Evaluate for Plasmodium parasites.
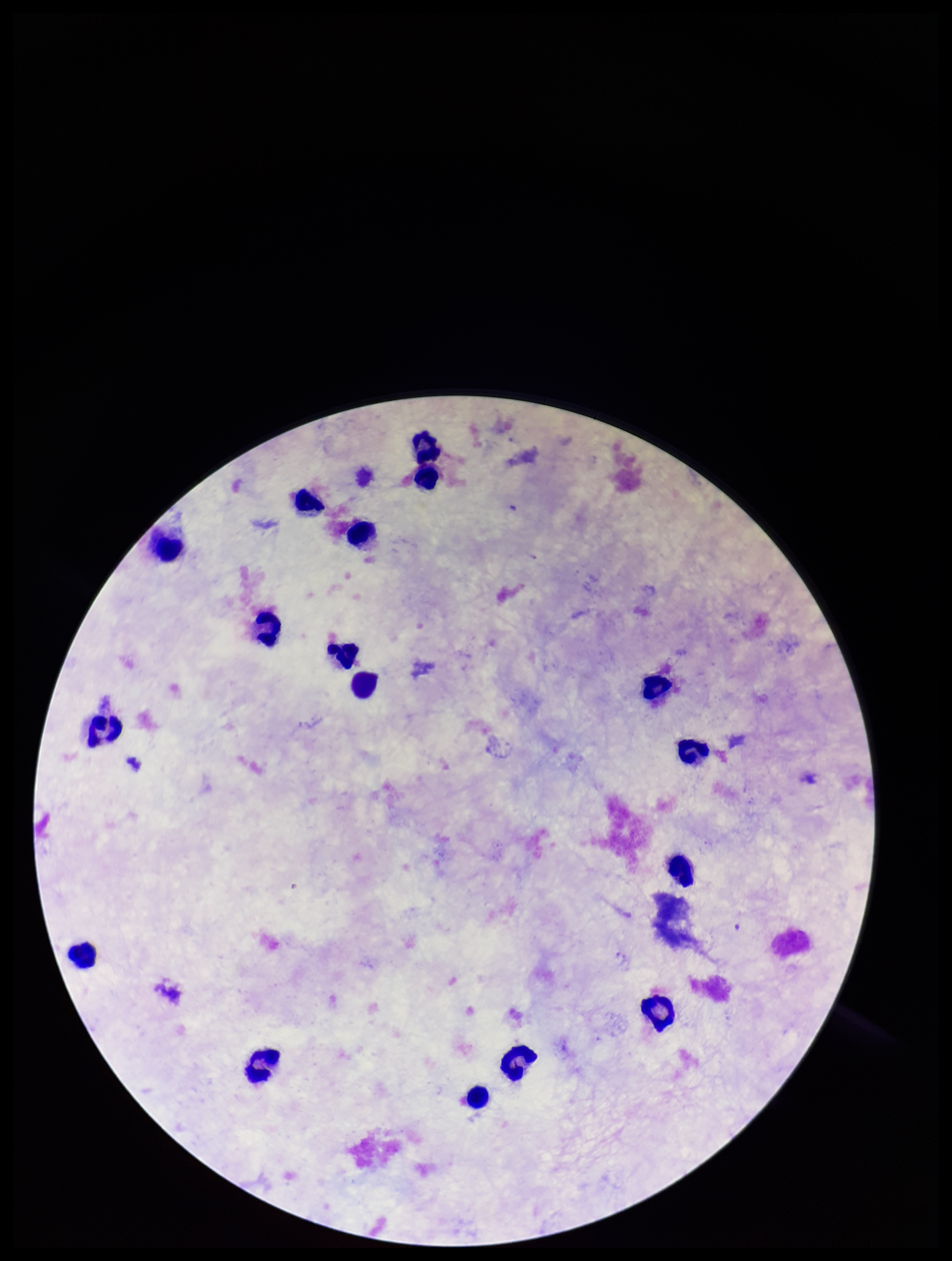
None identified.

Parasite count: 0. Image is 952×1261 pixels. Preparation: thick blood smear. Leukocyte count: 18. Smartphone photograph taken through the eyepiece of a microscope. One field from this slide. Patient malaria status: negative. Stained with Giemsa.